Comment on the morphology of the erythrocytes.
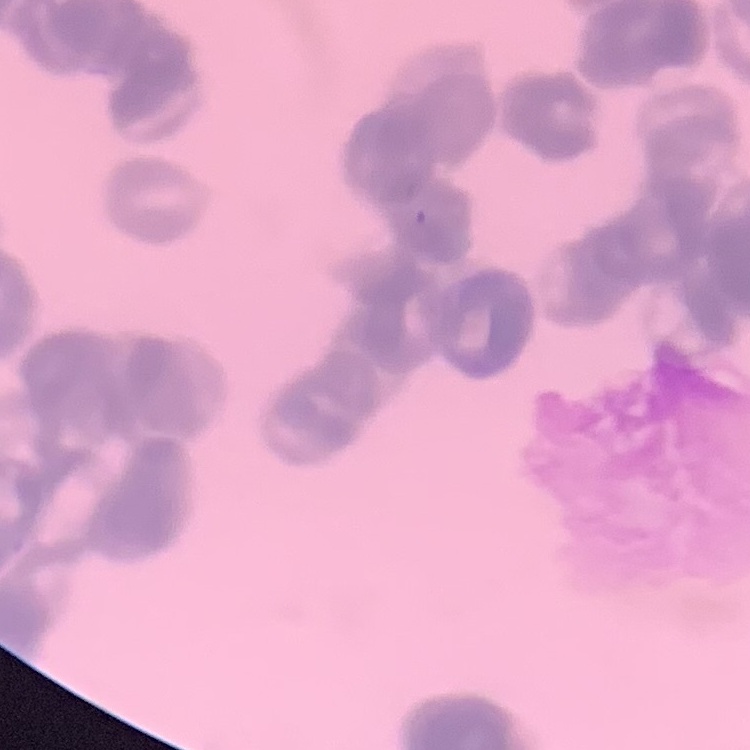
Rouleaux formation.

Thin blood smear. Field's or Giemsa stain. Square crop of a larger photomicrograph.